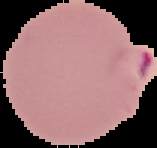

Summary:
  - Image type: cell region segmented out of the field of view; surrounding area masked to black
  - Preparation: thin blood film
  - Image size: 157×148 pixels
  - Malaria status: parasitized